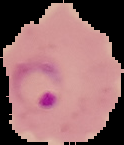
Summary:
  - Malaria status: parasitized
  - Image size: 124×145 pixels
  - Image type: cell region segmented out of the field of view; surrounding area masked to black
  - Preparation: thin blood smear